State which parasite is depicted.
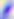

Toxoplasma gondii.

magnification: 400x
modality: micrograph